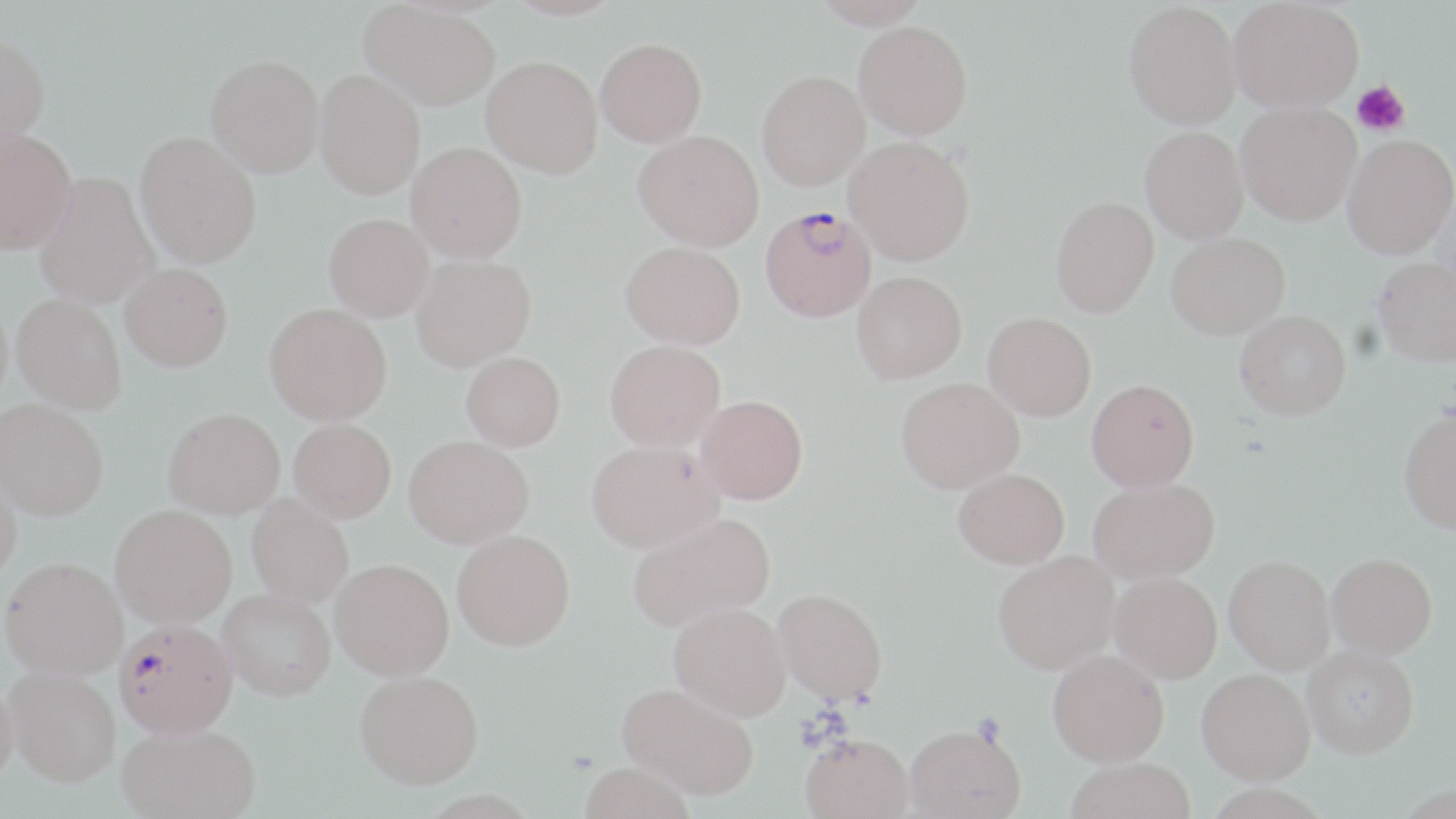

Approximate bounding boxes as (x1,y1)-(x2,y2) corner pairs in pixels. Platelet locations: (1351,81)-(1410,136). Uninfected red blood cell locations: (813,0)-(929,28), (1228,0)-(1364,113), (360,1)-(500,111), (1123,1)-(1241,129), (853,20)-(973,139), (0,32)-(50,154), (595,37)-(707,147), (205,55)-(324,176), (481,56)-(602,177), (314,69)-(425,199), (756,70)-(870,190), (1236,101)-(1362,225), (1140,127)-(1248,244), (0,129)-(77,254), (633,129)-(764,251), (135,131)-(261,268), (1342,134)-(1456,259), (844,136)-(975,265), (407,142)-(527,262), (34,172)-(159,310), (1431,185)-(1456,306), (1050,196)-(1159,318), (324,213)-(433,321), (1166,233)-(1290,338), (620,241)-(745,349), (411,253)-(536,371), (1373,257)-(1456,365), (120,263)-(233,371), (851,270)-(967,382), (11,294)-(126,415), (264,303)-(392,425), (1235,310)-(1351,419), (983,311)-(1096,420), (605,340)-(726,453), (461,353)-(566,453), (896,377)-(1024,493), (1086,378)-(1199,491), (696,395)-(808,505), (0,400)-(107,522), (1398,408)-(1456,534), (162,409)-(285,520), (288,420)-(396,525), (404,436)-(534,550), (586,442)-(723,556), (0,465)-(23,585), (953,467)-(1069,569), (1088,478)-(1219,584), (246,497)-(353,609), (110,506)-(237,630), (627,513)-(775,634), (452,532)-(576,654), (993,551)-(1120,674), (1327,553)-(1437,658), (1225,556)-(1335,673), (1,559)-(126,683), (329,561)-(454,682), (1110,572)-(1222,683), (773,589)-(888,707), (217,592)-(336,706), (668,604)-(791,723), (1303,646)-(1419,757), (1047,650)-(1169,766), (1197,668)-(1315,784), (5,672)-(121,792), (355,673)-(485,793), (0,684)-(20,791), (617,685)-(757,801), (905,724)-(1026,819), (118,727)-(261,819), (800,738)-(914,819), (1064,758)-(1196,819), (578,765)-(696,819). Plasmodium falciparum-infected red blood cell locations: (760,205)-(877,322), (115,622)-(238,743). Slide-level diagnosis: Plasmodium falciparum. May-Grünwald-Giemsa stain. One field of a larger specimen. Optical microscopy. Captured at 1000x magnification. Thin blood smear. Image is 1456×819 pixels.